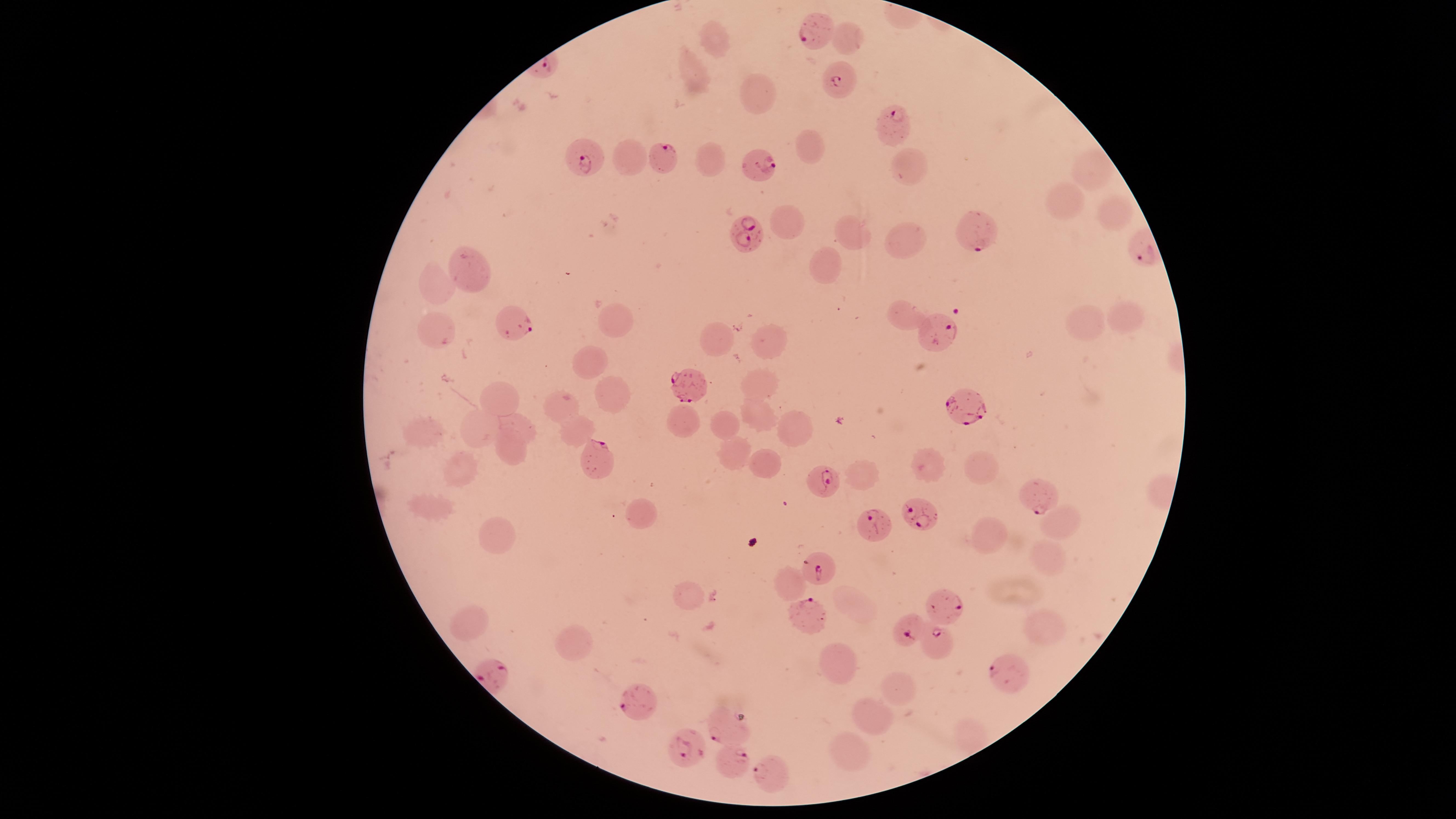

Approximate marker points, in pixels from the top-left corner.
Summary:
  - Uninfected red blood cells: (x=714, y=36), (x=694, y=67), (x=754, y=91), (x=803, y=143), (x=631, y=154), (x=704, y=162), (x=910, y=171), (x=1085, y=174), (x=1062, y=201), (x=1109, y=210), (x=786, y=216), (x=856, y=237), (x=908, y=240), (x=828, y=264), (x=466, y=268), (x=438, y=281), (x=902, y=316), (x=1118, y=316), (x=614, y=321), (x=1086, y=327), (x=437, y=332), (x=771, y=340), (x=721, y=341), (x=593, y=362), (x=762, y=379), (x=501, y=397), (x=614, y=397), (x=562, y=401), (x=757, y=415), (x=682, y=420), (x=721, y=420), (x=481, y=423), (x=519, y=426), (x=792, y=427), (x=420, y=431), (x=570, y=434), (x=736, y=446), (x=512, y=454), (x=761, y=461), (x=926, y=467), (x=979, y=467), (x=457, y=472), (x=864, y=478), (x=432, y=508), (x=646, y=515), (x=1059, y=523), (x=495, y=536), (x=994, y=538), (x=1043, y=555), (x=791, y=581), (x=684, y=596), (x=855, y=607), (x=469, y=616), (x=1040, y=629), (x=572, y=644), (x=834, y=661), (x=895, y=693), (x=872, y=714), (x=849, y=749)
  - Parasitized red blood cells: (x=818, y=31), (x=842, y=81), (x=891, y=123), (x=665, y=155), (x=591, y=158), (x=759, y=164), (x=975, y=230), (x=744, y=237), (x=518, y=324), (x=940, y=333), (x=680, y=383), (x=963, y=404), (x=595, y=459), (x=826, y=477), (x=1039, y=497), (x=923, y=514), (x=877, y=526), (x=822, y=566), (x=945, y=604), (x=810, y=614), (x=912, y=633), (x=933, y=644), (x=1012, y=675), (x=631, y=704), (x=718, y=728), (x=684, y=749), (x=736, y=764), (x=765, y=774)
  - Preparation: thin blood smear
  - Field of view: single
  - Visible region: circular
  - Image size: 1456×819 pixels
  - Presence: malaria parasites identified
  - Stain: Giemsa
  - Capture: smartphone photograph through the microscope eyepiece
  - Species: Plasmodium falciparum